Assess this cell for malaria.
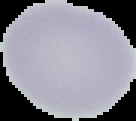
It is uninfected.

Summary:
  - Image type: segmented cell region with the area outside set to black
  - Image size: 136×121 pixels
  - Preparation: thin blood film